Classify this cell by malaria status.
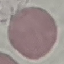

It is uninfected.

Summary:
  - Preparation: thin blood film
  - Capture: smartphone through the microscope eyepiece
  - Stain: Giemsa
  - Image type: automatically extracted cell patch, resized to 64 × 64 pixels